Identify the parasite.
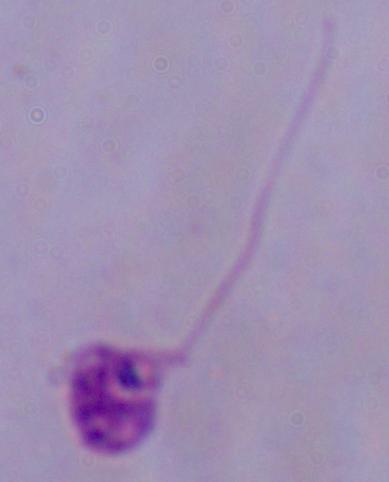
Leishmania.

Summary:
  - Magnification: 1000x
  - Modality: photomicrograph